State the blood parasite species.
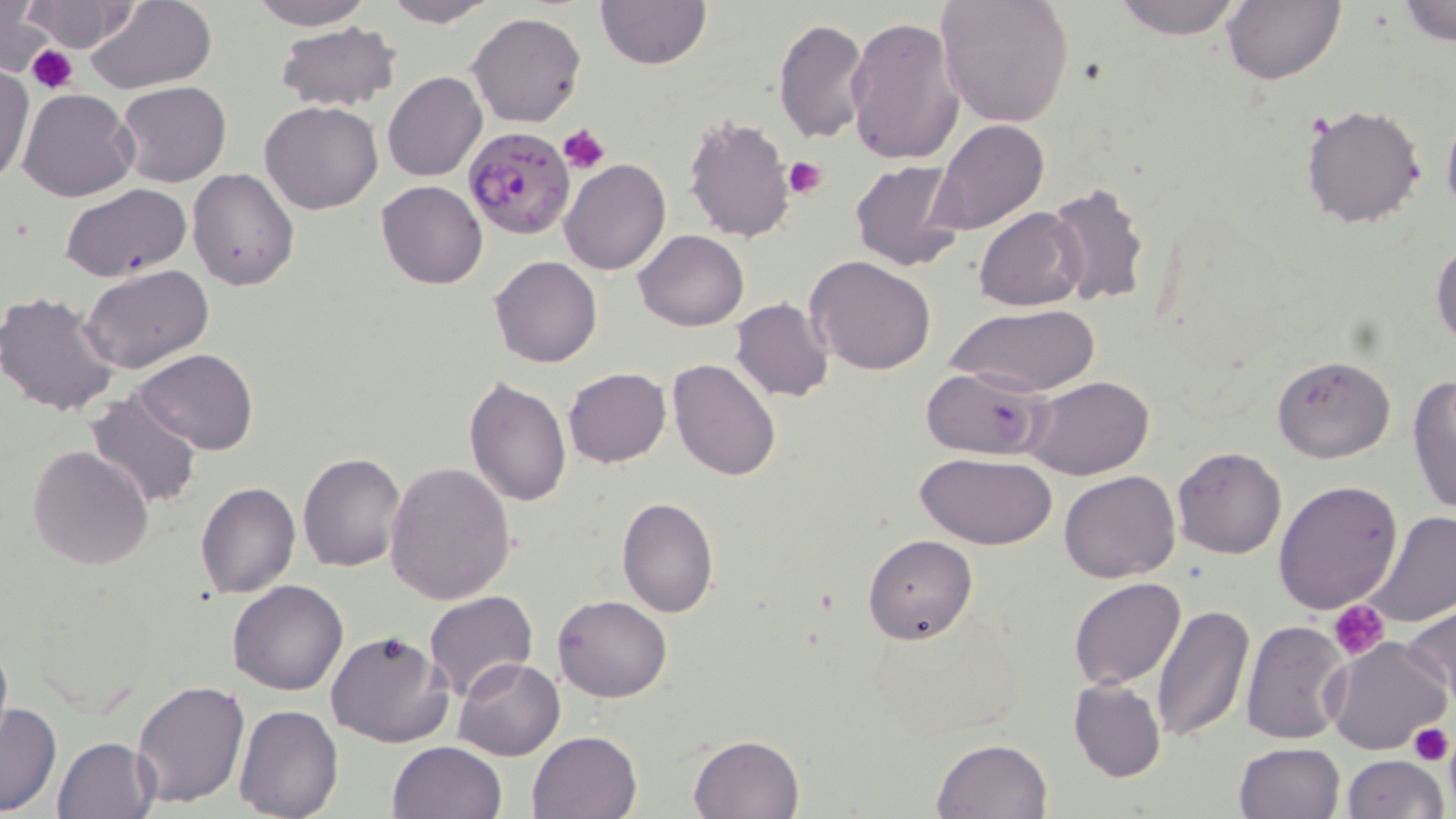
Plasmodium falciparum.

stain = May-Grünwald-Giemsa
image size = 1456×819 pixels
uninfected red blood cell locations = approximate bounding boxes as (x1,y1)-(x2,y2) corner pairs in pixels: (245,0)-(373,30), (382,0)-(501,27), (595,0)-(710,69), (936,0)-(1075,128), (1110,0)-(1247,40), (1222,0)-(1346,85), (1397,0)-(1456,48), (22,1)-(139,52), (84,1)-(216,94), (0,2)-(52,74), (468,12)-(587,128), (844,15)-(963,166), (775,18)-(869,143), (275,24)-(401,111), (0,67)-(34,185), (383,71)-(486,181), (116,80)-(231,187), (18,89)-(138,202), (261,102)-(383,215), (1300,102)-(1427,230), (1442,110)-(1456,226), (683,114)-(795,244), (932,120)-(1050,236), (560,159)-(670,275), (849,160)-(966,273), (188,168)-(300,293), (377,180)-(487,289), (1045,180)-(1153,311), (61,184)-(192,282), (975,207)-(1088,311), (634,230)-(749,330), (1431,239)-(1456,349), (804,255)-(935,376), (491,256)-(600,368), (80,264)-(214,374), (96,283)-(229,435), (0,290)-(122,415), (731,298)-(834,402), (948,303)-(1101,397), (132,350)-(257,454), (1271,355)-(1396,463), (668,358)-(779,481), (563,367)-(670,467), (922,367)-(1049,459), (1407,372)-(1456,518), (465,375)-(571,506), (1024,375)-(1155,480), (84,391)-(202,511), (27,445)-(154,570), (1173,447)-(1287,559), (298,452)-(406,571), (917,452)-(1060,549), (385,460)-(515,603), (1060,469)-(1181,583), (1274,480)-(1404,614), (196,482)-(300,599), (617,497)-(719,618), (1362,510)-(1456,628), (863,535)-(976,643), (1068,576)-(1185,690), (228,580)-(348,696), (424,591)-(537,703), (554,595)-(672,702), (1152,600)-(1254,745), (1402,601)-(1456,705), (1240,620)-(1351,745), (326,631)-(453,748), (0,634)-(12,746), (1326,636)-(1453,756), (453,658)-(564,760), (1068,677)-(1166,783), (132,680)-(250,808), (1,704)-(62,816), (233,705)-(343,819), (528,729)-(642,819), (690,733)-(802,818), (52,736)-(160,819), (932,738)-(1054,819), (387,740)-(507,819), (1232,741)-(1344,819), (1342,754)-(1448,818)
field of view = single
platelet locations = approximate bounding boxes as (x1,y1)-(x2,y2) corner pairs in pixels: (28,45)-(78,95), (558,124)-(610,175), (782,155)-(826,202), (1328,599)-(1390,661), (1409,723)-(1453,765)
preparation = thin blood smear
modality = light microscopy
Plasmodium falciparum-infected red blood cell locations = approximate bounding boxes as (x1,y1)-(x2,y2) corner pairs in pixels: (464,126)-(573,238)
magnification = 1000x